Point out each leukocyte.
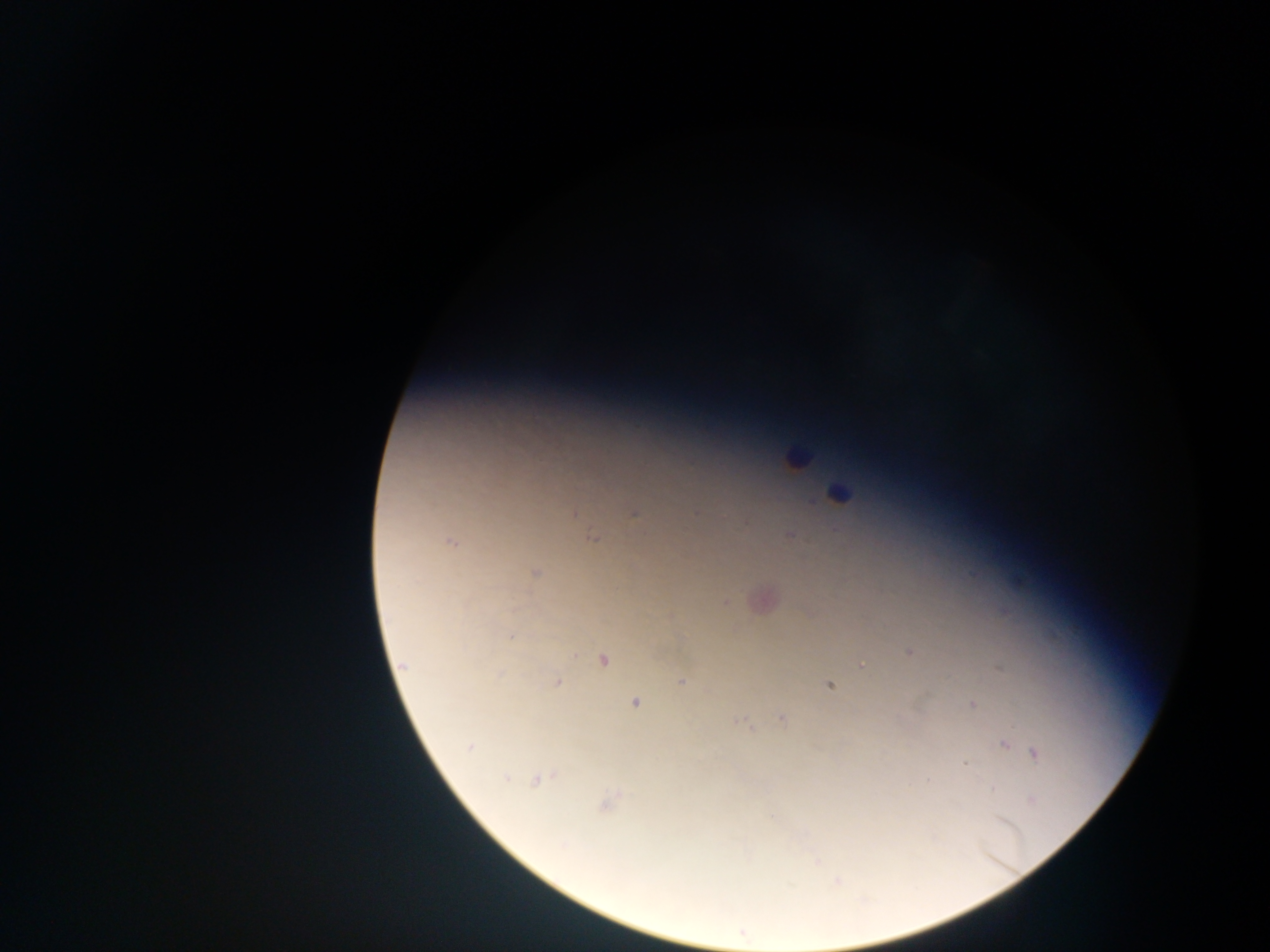

Approximate centers as {x, y} in pixels.
Leukocytes: {794, 458}, {837, 494}.

malaria parasite locations = approximate centers as {x, y} in pixels: {573, 512}, {634, 512}, {789, 535}, {592, 537}, {450, 542}, {534, 573}, {760, 598}, {723, 602}, {909, 652}, {602, 659}, {861, 664}, {402, 665}, {682, 680}, {556, 682}, {829, 685}, {635, 702}, {972, 704}, {781, 717}, {741, 722}, {1003, 744}, {470, 747}, {1035, 754}, {964, 764}, {537, 779}, {606, 801}, {836, 882}, {741, 932}
capture = mobile-phone photograph through a microscope
country = Ghana
image size = 1270×952 pixels
field of view = single
preparation = thick blood smear